Assess this cell for malaria.
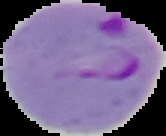

It is parasitized.

Summary:
  - Image type: segmented cell region with the area outside set to black
  - Image size: 166×136 pixels
  - Preparation: thin blood smear